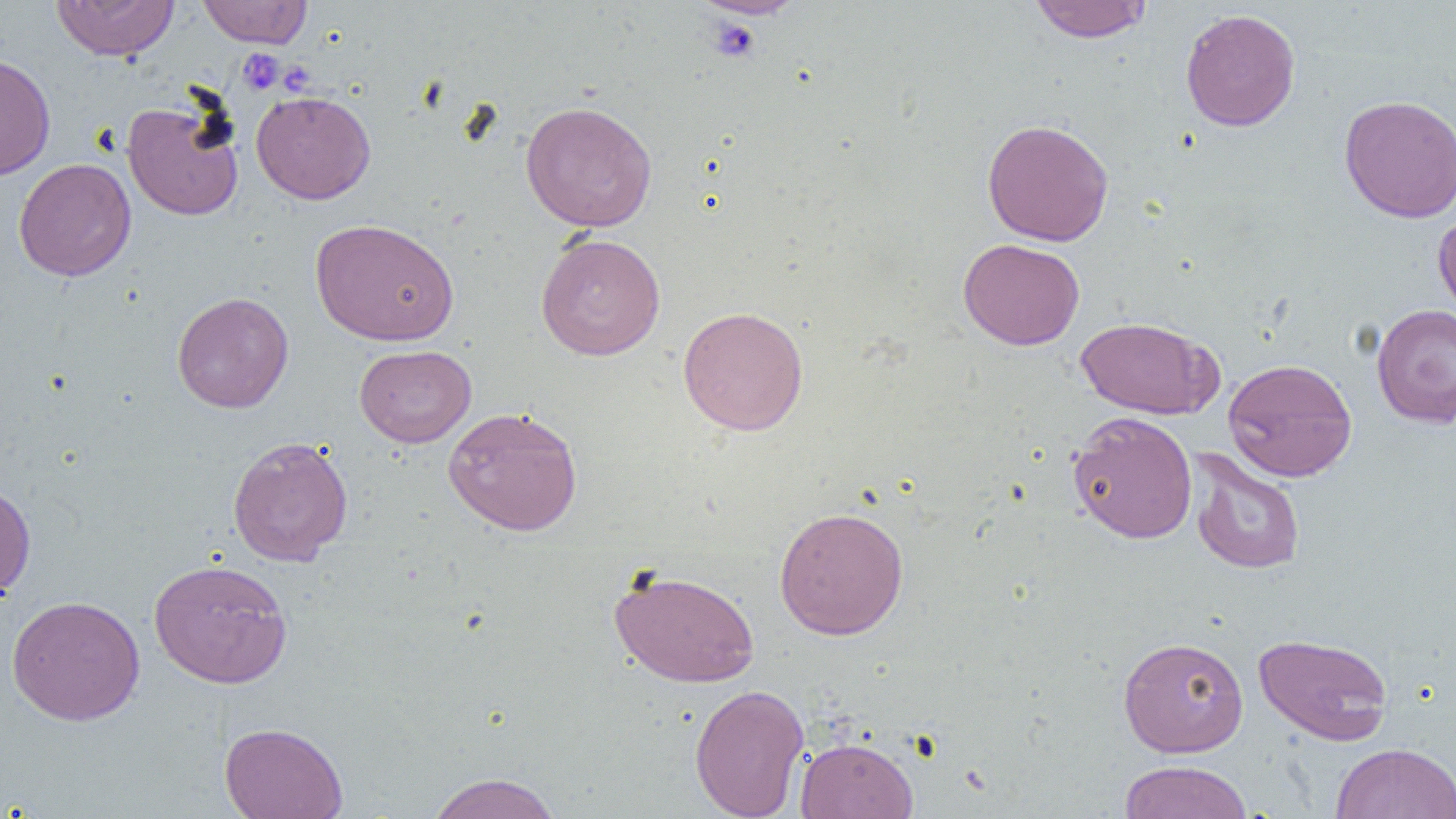
slide-level diagnosis = negative for blood parasites
uninfected red blood cell locations = approximate bounding boxes as (x1,y1)-(x2,y2) corner pairs in pixels: (50,0)-(180,61), (692,0)-(808,20), (1029,0)-(1152,43), (197,1)-(312,48), (1180,8)-(1301,132), (0,53)-(56,180), (251,90)-(376,204), (1338,94)-(1456,223), (122,99)-(244,221), (519,100)-(657,232), (981,118)-(1114,246), (14,158)-(136,282), (1433,211)-(1456,325), (310,218)-(459,346), (535,233)-(666,361), (958,238)-(1085,350), (171,292)-(294,413), (1371,304)-(1456,429), (677,306)-(809,436), (1075,316)-(1221,419), (354,345)-(476,447), (1222,357)-(1357,482), (442,405)-(583,536), (1068,411)-(1197,544), (228,435)-(353,566), (1187,448)-(1306,575), (0,481)-(36,602), (774,506)-(909,640), (149,558)-(292,688), (608,566)-(761,687), (6,595)-(146,725), (1254,633)-(1393,745), (1118,635)-(1249,758), (689,683)-(809,818), (219,721)-(348,819), (795,737)-(918,818), (1330,742)-(1456,819), (1118,759)-(1253,819), (425,772)-(563,819)
field of view = single
preparation = thin blood smear
image size = 1456×819 pixels
modality = light microscopy
platelet locations = approximate bounding boxes as (x1,y1)-(x2,y2) corner pairs in pixels: (706,18)-(762,62), (237,49)-(283,94)
magnification = 1000x